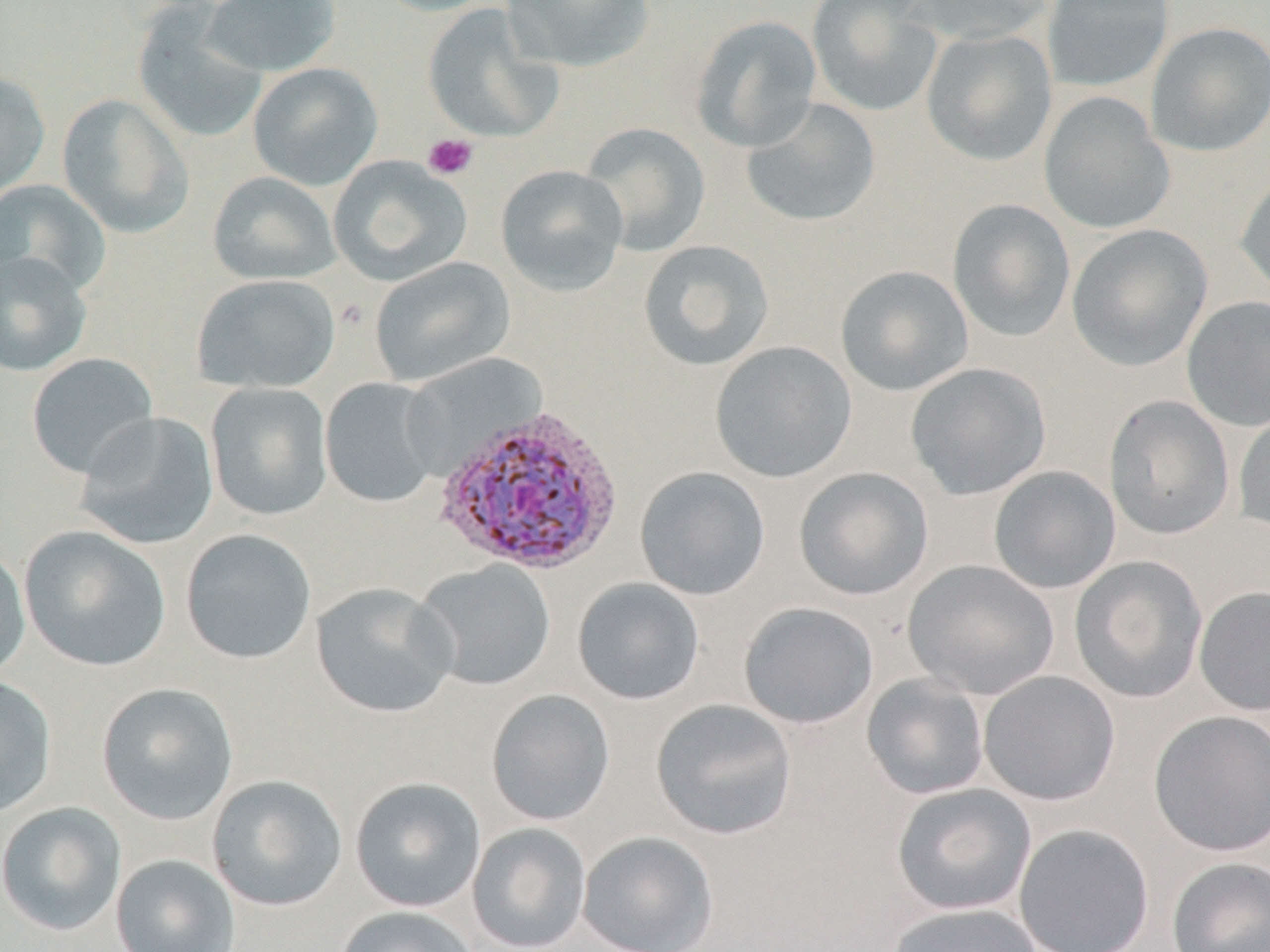
slide_level_diagnosis: Plasmodium vivax
stain: May-Grünwald-Giemsa
plasmodium_vivax_infected_red_blood_cell_locations: 'approximate bounding boxes as [x1, y1, x2, y2] in pixels: [431, 402, 626, 578]'
modality: light microscopy
magnification: 1000x
image_size: 1270×952 pixels
uninfected_red_blood_cell_locations: 'approximate bounding boxes as [x1, y1, x2, y2] in pixels: [201, 0, 341, 77], [369, 0, 500, 17], [501, 0, 656, 72], [807, 0, 943, 117], [906, 0, 1058, 46], [1042, 0, 1175, 92], [132, 3, 270, 145], [422, 3, 562, 144], [691, 15, 822, 153], [1146, 21, 1270, 157], [921, 28, 1057, 167], [247, 62, 383, 191], [0, 69, 50, 200], [1039, 92, 1175, 234], [57, 93, 195, 238], [741, 98, 882, 228], [579, 122, 711, 256], [327, 155, 472, 286], [495, 164, 629, 296], [207, 171, 341, 286], [1234, 171, 1270, 300], [0, 179, 113, 299], [947, 198, 1075, 343], [1066, 224, 1212, 372], [638, 239, 775, 372], [0, 251, 92, 376], [369, 256, 515, 387], [835, 265, 973, 397], [192, 274, 340, 394], [1182, 295, 1270, 431], [709, 340, 857, 484], [26, 353, 159, 479], [906, 362, 1051, 500], [320, 377, 442, 508], [205, 383, 333, 521], [1104, 395, 1235, 540], [1233, 407, 1270, 535], [74, 412, 220, 551], [988, 465, 1121, 594], [635, 467, 770, 601], [794, 467, 933, 601], [18, 525, 170, 672], [180, 529, 316, 665], [0, 545, 31, 682], [1069, 555, 1208, 703], [903, 559, 1059, 700], [414, 560, 556, 691], [572, 577, 705, 705], [311, 582, 458, 719], [1194, 586, 1270, 716], [739, 601, 878, 729], [978, 670, 1120, 807], [861, 674, 990, 800], [0, 676, 57, 817], [96, 682, 239, 826], [486, 689, 615, 826], [650, 699, 798, 840], [1148, 710, 1270, 857], [207, 774, 347, 912], [349, 777, 486, 913], [891, 783, 1037, 916], [0, 802, 126, 936], [466, 822, 591, 952], [1013, 823, 1154, 952], [577, 831, 719, 952], [110, 854, 240, 952], [1166, 856, 1270, 952], [884, 902, 1048, 952], [333, 905, 479, 952]'
preparation: thin blood smear
platelet_locations: 'approximate bounding boxes as [x1, y1, x2, y2] in pixels: [422, 133, 478, 181]'
field_of_view: one of a larger specimen